Outline each blood parasite and name the species.
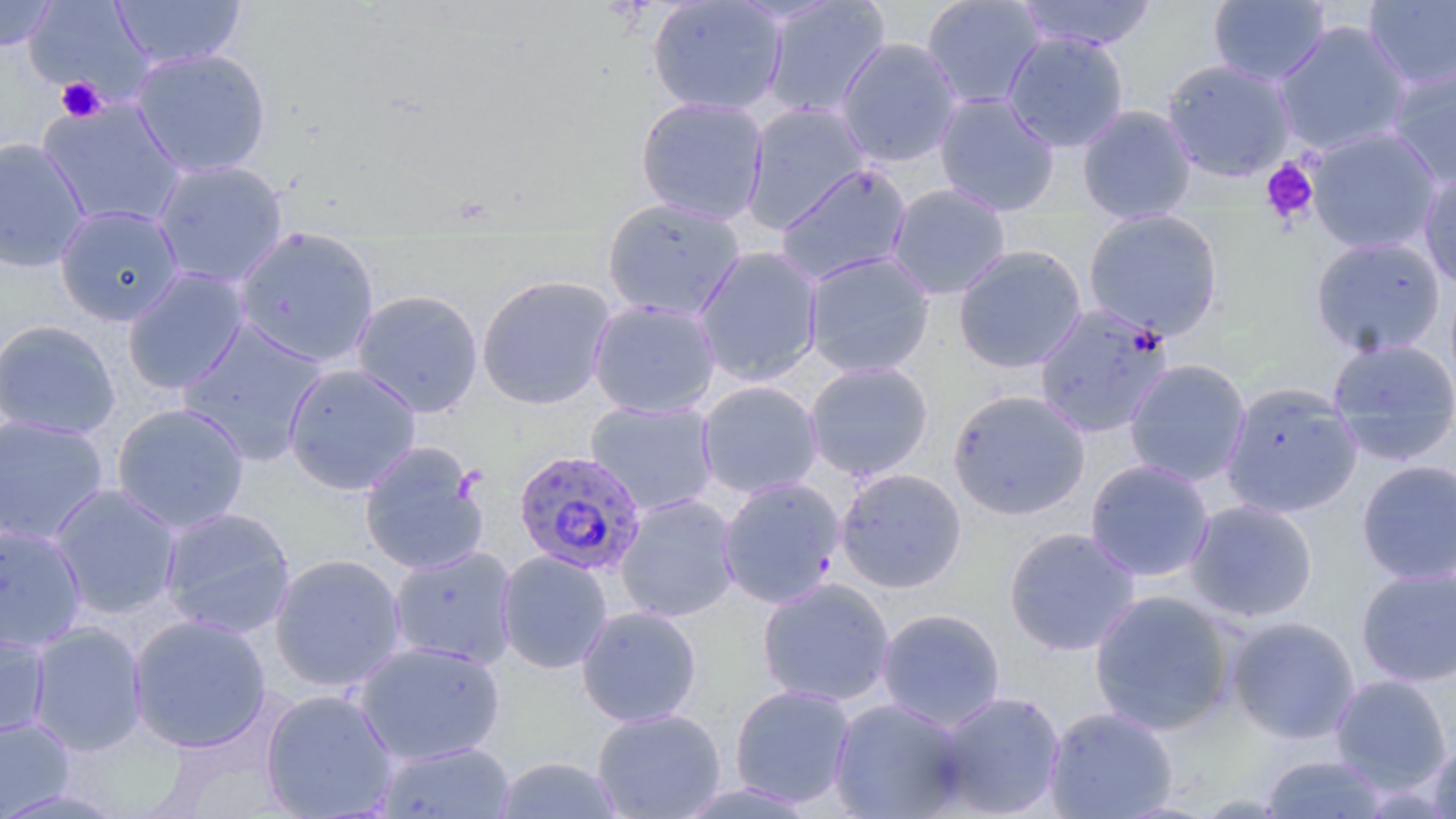

Approximate bounding boxes as (x1, y1, x2, y2) in pixels.
Plasmodium falciparum-infected red blood cells: (1034, 301, 1174, 438), (513, 449, 647, 576).
No Plasmodium ovale, Plasmodium malariae, Plasmodium vivax, Babesia divergens, or Trypanosoma brucei observed.

Platelet locations: (56, 77, 106, 123), (1260, 158, 1320, 225). Uninfected red blood cell locations: (0, 0, 60, 52), (23, 0, 155, 103), (646, 0, 787, 116), (920, 0, 1047, 110), (1012, 0, 1158, 51), (1207, 0, 1331, 86), (111, 1, 246, 71), (761, 1, 890, 119), (1363, 1, 1456, 91), (1273, 20, 1414, 157), (1002, 31, 1130, 153), (835, 37, 963, 167), (130, 47, 273, 179), (1161, 58, 1298, 182), (1385, 60, 1456, 191), (933, 91, 1060, 217), (634, 96, 770, 225), (37, 97, 187, 230), (740, 102, 872, 233), (1076, 104, 1197, 224), (1305, 126, 1443, 255), (0, 137, 91, 273), (151, 159, 289, 288), (775, 163, 913, 285), (1418, 169, 1456, 292), (885, 183, 1012, 300), (601, 197, 746, 322), (54, 204, 184, 326), (1082, 209, 1224, 341), (233, 228, 381, 368), (1310, 235, 1447, 358), (952, 245, 1087, 373), (693, 246, 824, 387), (803, 251, 935, 379), (121, 267, 250, 396), (476, 274, 616, 410), (350, 289, 484, 418), (587, 298, 721, 419), (0, 319, 121, 440), (177, 320, 329, 465), (1327, 337, 1456, 464), (1123, 358, 1252, 487), (803, 360, 934, 481), (282, 362, 422, 497), (696, 380, 824, 499), (1220, 382, 1363, 519), (948, 389, 1090, 520), (585, 400, 720, 517), (111, 402, 250, 534), (0, 414, 110, 546), (358, 441, 489, 576), (1084, 458, 1216, 582), (1356, 459, 1455, 585), (834, 468, 967, 593), (717, 477, 846, 609), (48, 484, 183, 620), (615, 493, 740, 623), (1184, 499, 1319, 623), (157, 507, 296, 639), (0, 522, 87, 652), (1003, 526, 1142, 656), (388, 546, 518, 670), (496, 550, 613, 674), (269, 553, 407, 692), (1355, 566, 1456, 687), (757, 577, 895, 707), (1088, 589, 1237, 736), (576, 606, 703, 727), (876, 608, 1006, 731), (127, 614, 271, 753), (1226, 615, 1361, 744), (27, 622, 148, 756), (0, 623, 51, 741), (352, 641, 506, 765), (1329, 674, 1453, 793), (729, 684, 857, 808), (260, 689, 399, 819), (933, 691, 1066, 817), (827, 697, 968, 818), (1043, 706, 1178, 818), (591, 708, 726, 818), (0, 714, 76, 818), (1428, 739, 1456, 819), (374, 741, 516, 819), (1259, 754, 1389, 818), (495, 757, 625, 817). Slide-level diagnosis: Plasmodium falciparum. Light microscopy. 1000x magnification. Thin blood smear. May-Grünwald-Giemsa-stained preparation. Image is 1456×819 pixels. One field of a larger specimen.